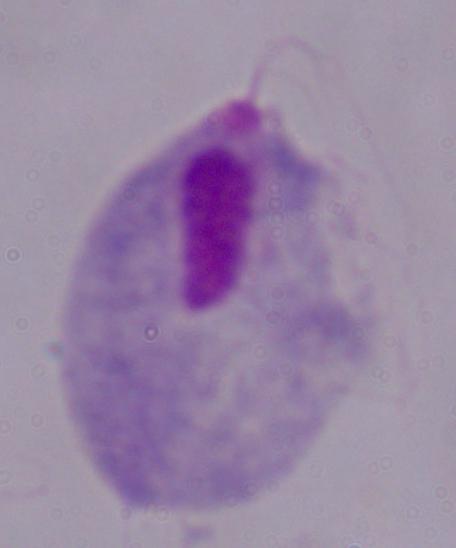 Photomicrograph. A trichomonad is seen. 1000x magnification.